Assess this cell for malaria.
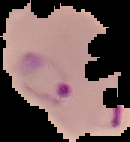
It is parasitized.

From a thin blood film. Image is 130×142 pixels. The area outside the segmented cell region is set to black.